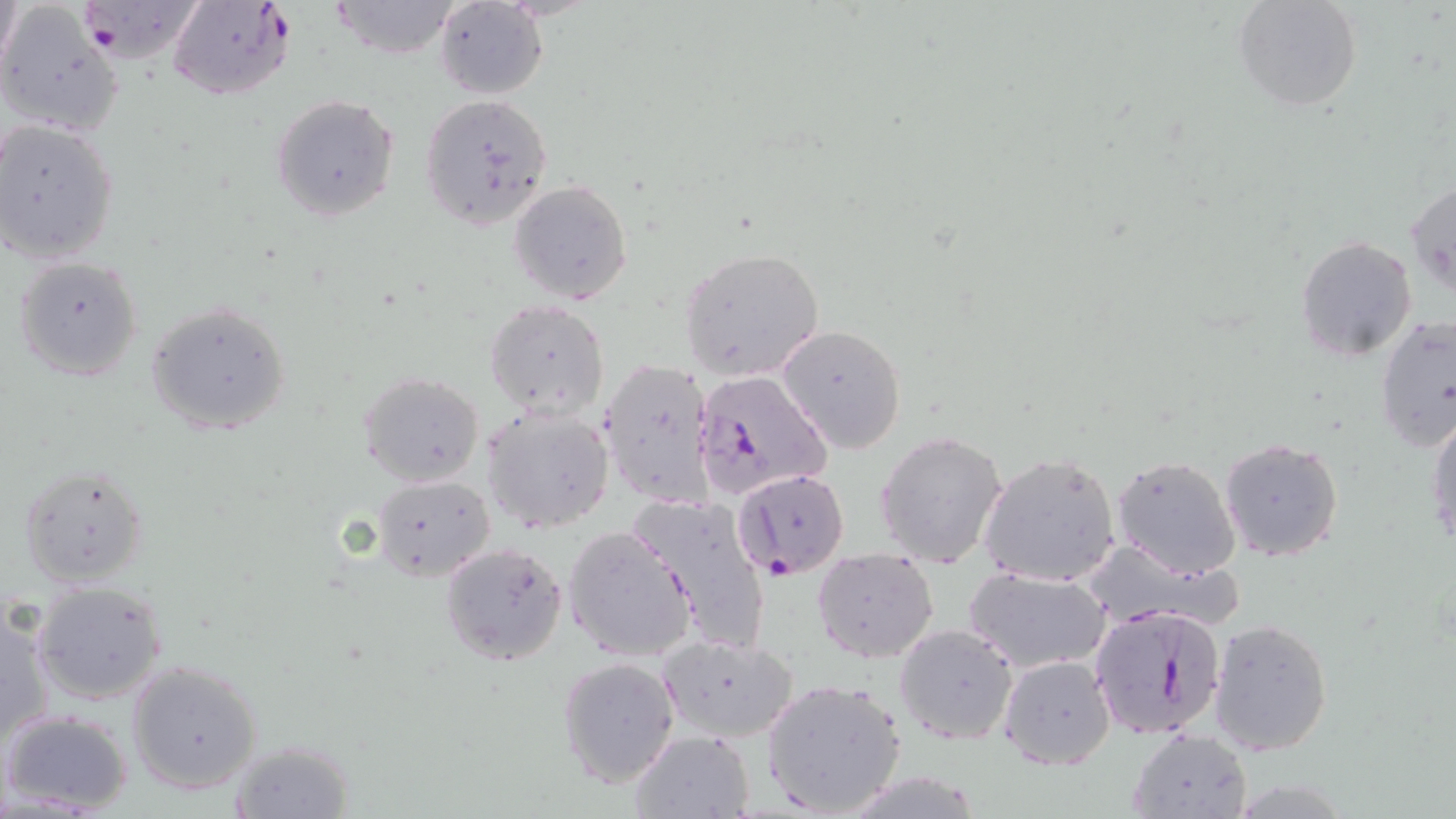
Approximate bounding boxes as [x1, y1, x2, y2] in pixels. Plasmodium falciparum-infected red blood cell locations: [72, 0, 203, 64], [170, 1, 293, 101], [694, 367, 831, 499], [734, 470, 850, 579], [1087, 605, 1228, 740]. Uninfected red blood cell locations: [1233, 0, 1362, 113], [328, 1, 463, 59], [433, 2, 548, 98], [0, 4, 122, 136], [418, 92, 554, 232], [269, 93, 400, 223], [1, 120, 120, 264], [1407, 178, 1455, 299], [508, 180, 632, 304], [1296, 235, 1418, 361], [679, 247, 824, 380], [13, 255, 144, 382], [486, 298, 609, 420], [146, 301, 291, 436], [1375, 316, 1456, 452], [778, 323, 908, 454], [599, 355, 718, 510], [358, 371, 485, 487], [483, 406, 613, 532], [1426, 410, 1456, 554], [874, 429, 1008, 570], [1219, 436, 1345, 561], [977, 452, 1122, 589], [1111, 453, 1243, 578], [18, 464, 150, 589], [370, 475, 496, 579], [633, 494, 775, 651], [563, 524, 697, 662], [439, 541, 569, 666], [1093, 543, 1244, 626], [811, 547, 939, 664], [965, 568, 1111, 673], [30, 580, 168, 705], [1, 600, 54, 741], [1208, 617, 1333, 755], [893, 623, 1019, 746], [658, 632, 800, 743], [999, 654, 1115, 771], [557, 656, 680, 787], [128, 660, 264, 794], [759, 676, 908, 818], [2, 709, 135, 815], [629, 728, 754, 819], [1127, 728, 1252, 818], [226, 740, 357, 818]. Slide-level diagnosis: Plasmodium falciparum. Optical microscopy. Captured at 1000x magnification. Image is 1456×819 pixels. One field of a larger specimen. May-Grünwald-Giemsa stain. Thin blood smear.